Locate and identify every blood parasite.
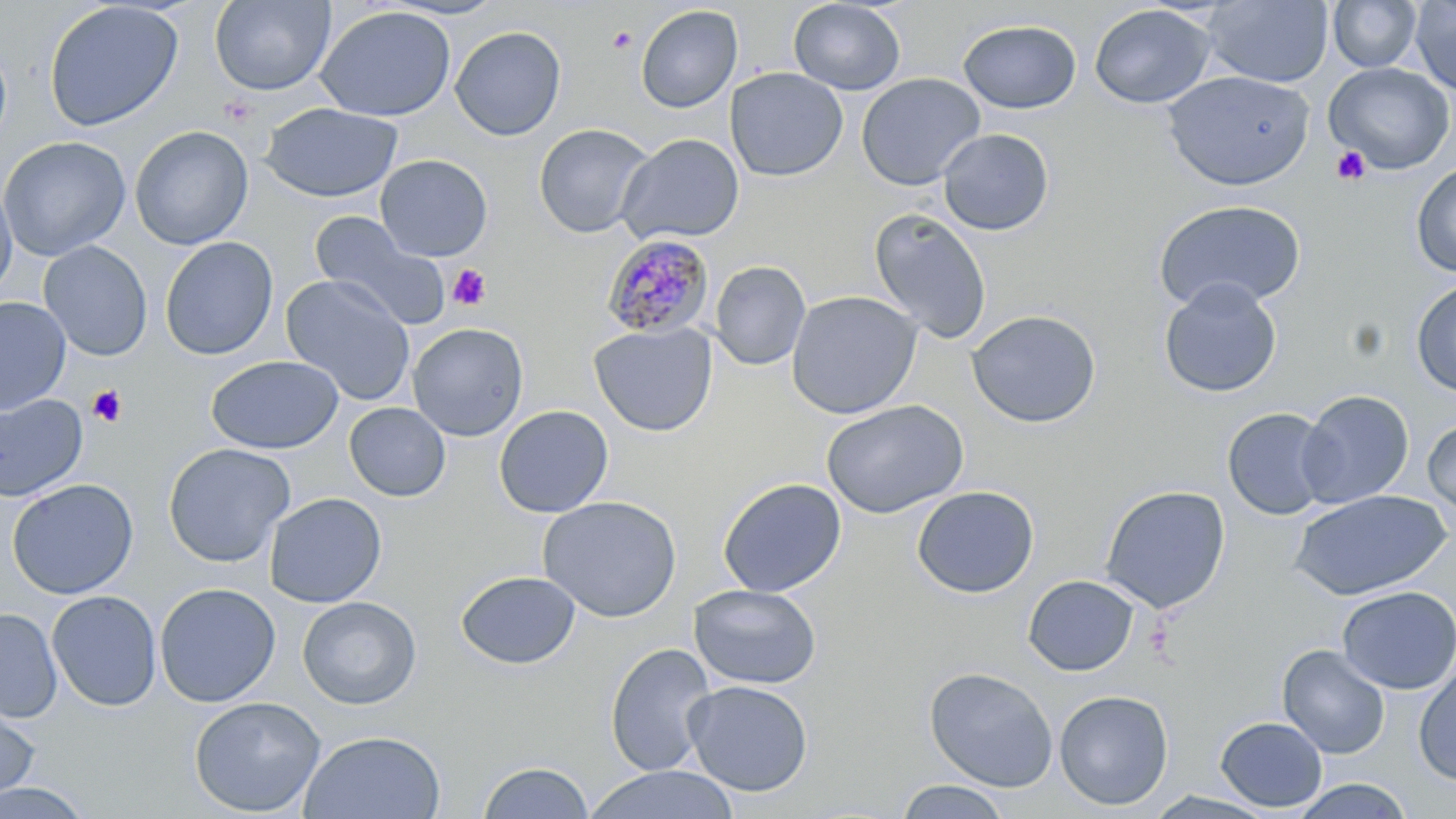
Approximate bounding boxes as [x1, y1, x2, y2] in pixels.
Plasmodium malariae-infected red blood cells: [601, 233, 715, 341].
No Plasmodium falciparum, Plasmodium ovale, Plasmodium vivax, Babesia divergens, or Trypanosoma brucei observed.

slide_level_diagnosis: Plasmodium malariae
stain: May-Grünwald-Giemsa
uninfected_red_blood_cell_locations: 'approximate bounding boxes as [x1, y1, x2, y2] in pixels: [210, 0, 335, 96], [382, 0, 509, 20], [1201, 0, 1333, 87], [1327, 0, 1422, 72], [43, 1, 184, 132], [788, 1, 906, 94], [1409, 1, 1456, 96], [1089, 4, 1216, 108], [635, 5, 743, 113], [315, 6, 456, 122], [958, 19, 1081, 114], [450, 25, 567, 141], [0, 39, 12, 154], [1324, 62, 1455, 174], [724, 67, 848, 182], [1162, 70, 1315, 191], [856, 73, 985, 191], [261, 102, 402, 203], [533, 123, 654, 237], [130, 126, 253, 250], [937, 128, 1054, 236], [615, 133, 745, 246], [0, 136, 131, 262], [375, 154, 493, 261], [1411, 161, 1456, 278], [0, 179, 17, 300], [1153, 200, 1307, 313], [868, 208, 993, 345], [309, 212, 451, 330], [160, 236, 278, 360], [38, 241, 152, 361], [709, 261, 811, 370], [280, 274, 417, 406], [1157, 278, 1283, 398], [1411, 279, 1456, 398], [786, 290, 922, 419], [0, 297, 71, 413], [966, 309, 1102, 428], [407, 322, 528, 441], [589, 323, 717, 437], [206, 355, 343, 454], [1297, 389, 1414, 508], [0, 393, 88, 501], [822, 400, 969, 519], [344, 402, 450, 501], [494, 405, 613, 518], [1222, 408, 1337, 520], [1422, 418, 1456, 517], [162, 442, 296, 567], [7, 478, 138, 599], [717, 478, 847, 598], [1100, 484, 1231, 614], [911, 485, 1039, 598], [1289, 489, 1452, 600], [264, 492, 387, 608], [537, 495, 682, 622], [455, 570, 580, 669], [1023, 574, 1140, 677], [154, 582, 281, 707], [689, 584, 822, 689], [1337, 586, 1456, 695], [46, 589, 162, 711], [297, 596, 421, 709], [0, 608, 62, 723], [605, 642, 717, 776], [1277, 644, 1390, 759], [1413, 664, 1456, 786], [923, 666, 1058, 792], [683, 679, 813, 796], [1054, 689, 1174, 811], [188, 695, 326, 817], [0, 697, 42, 808], [1215, 716, 1328, 812], [298, 730, 447, 818], [477, 760, 594, 819], [584, 765, 741, 819], [1291, 778, 1414, 818], [895, 779, 1012, 818], [0, 780, 94, 818]'
platelet_locations: 'approximate bounding boxes as [x1, y1, x2, y2] in pixels: [607, 27, 638, 53], [1331, 146, 1371, 185], [448, 264, 491, 311], [87, 385, 128, 427]'
field_of_view: single
modality: light microscopy
preparation: thin blood film
magnification: 1000x
image_size: 1456×819 pixels